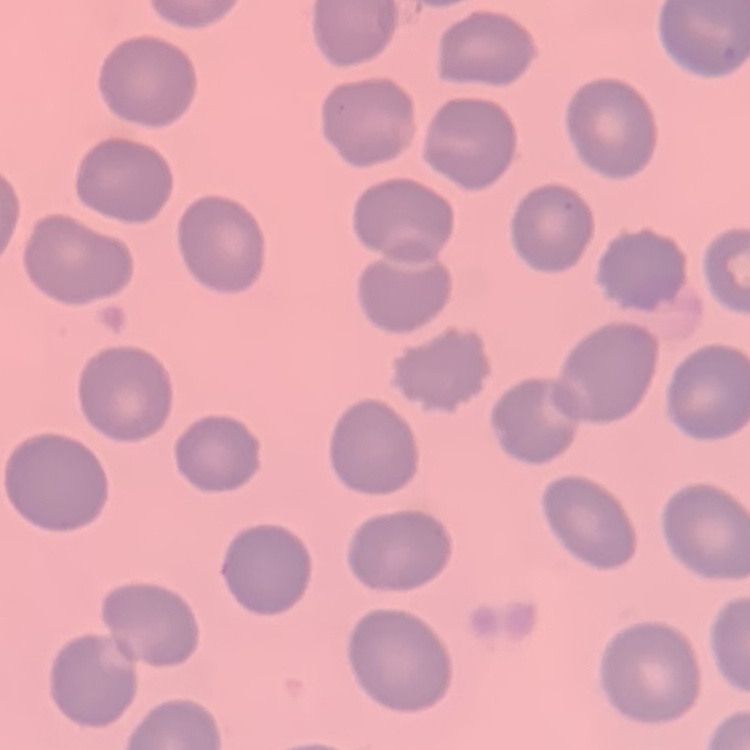
Summary:
  - Red blood cell morphology: no rouleaux formation
  - Preparation: thin blood film
  - Stain: Field's or Giemsa
  - Image type: one tile cut from a larger photomicrograph